Outline each blood parasite and name the species.
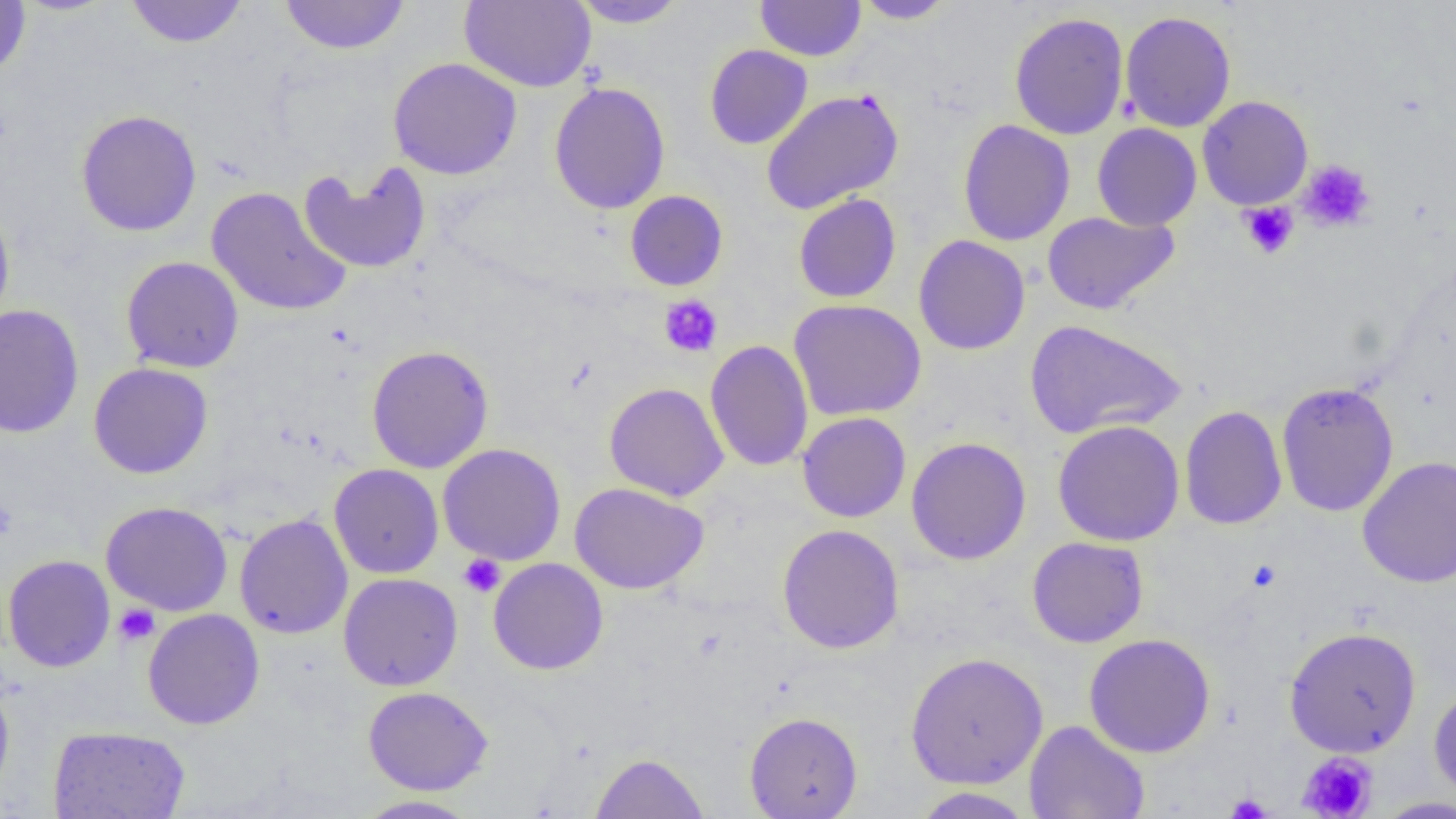
No blood parasites seen.

slide-level diagnosis = no evidence of blood parasites
platelet locations = approximate bounding boxes as named x1/y1/x2/y2 corners in pixels: (x1=1298, y1=160, x2=1376, y2=233), (x1=1238, y1=201, x2=1299, y2=260), (x1=658, y1=294, x2=723, y2=358), (x1=0, y1=497, x2=18, y2=541), (x1=458, y1=554, x2=506, y2=597), (x1=114, y1=604, x2=160, y2=646), (x1=1298, y1=752, x2=1377, y2=818), (x1=1226, y1=793, x2=1272, y2=818)
modality = optical microscopy
uninfected red blood cell locations = approximate bounding boxes as named x1/y1/x2/y2 corners in pixels: (x1=124, y1=0, x2=249, y2=49), (x1=280, y1=0, x2=410, y2=55), (x1=459, y1=0, x2=596, y2=92), (x1=570, y1=0, x2=689, y2=28), (x1=755, y1=0, x2=866, y2=61), (x1=853, y1=0, x2=957, y2=24), (x1=0, y1=1, x2=31, y2=78), (x1=1120, y1=10, x2=1236, y2=133), (x1=1009, y1=12, x2=1129, y2=140), (x1=704, y1=44, x2=813, y2=149), (x1=388, y1=57, x2=523, y2=179), (x1=549, y1=82, x2=671, y2=214), (x1=761, y1=88, x2=903, y2=215), (x1=1197, y1=95, x2=1313, y2=210), (x1=75, y1=109, x2=202, y2=237), (x1=958, y1=119, x2=1075, y2=247), (x1=1091, y1=123, x2=1202, y2=231), (x1=298, y1=161, x2=432, y2=274), (x1=206, y1=186, x2=352, y2=317), (x1=625, y1=190, x2=728, y2=291), (x1=793, y1=194, x2=902, y2=303), (x1=0, y1=199, x2=15, y2=330), (x1=1042, y1=210, x2=1179, y2=314), (x1=914, y1=235, x2=1030, y2=355), (x1=121, y1=255, x2=244, y2=373), (x1=788, y1=299, x2=926, y2=421), (x1=0, y1=304, x2=84, y2=439), (x1=1024, y1=319, x2=1186, y2=440), (x1=705, y1=340, x2=814, y2=471), (x1=366, y1=344, x2=494, y2=474), (x1=88, y1=362, x2=214, y2=479), (x1=1276, y1=381, x2=1399, y2=517), (x1=604, y1=382, x2=729, y2=502), (x1=1179, y1=405, x2=1287, y2=530), (x1=797, y1=411, x2=912, y2=523), (x1=1052, y1=420, x2=1184, y2=546), (x1=906, y1=436, x2=1031, y2=565), (x1=438, y1=443, x2=567, y2=566), (x1=1357, y1=456, x2=1456, y2=588), (x1=329, y1=463, x2=444, y2=579), (x1=570, y1=481, x2=709, y2=594), (x1=100, y1=501, x2=233, y2=616), (x1=234, y1=513, x2=353, y2=639), (x1=777, y1=524, x2=905, y2=654), (x1=1027, y1=536, x2=1149, y2=648), (x1=2, y1=554, x2=116, y2=672), (x1=487, y1=558, x2=609, y2=675), (x1=338, y1=572, x2=463, y2=691), (x1=142, y1=608, x2=265, y2=729), (x1=1283, y1=626, x2=1422, y2=757), (x1=1083, y1=633, x2=1216, y2=758), (x1=904, y1=651, x2=1049, y2=790), (x1=0, y1=675, x2=15, y2=802), (x1=1428, y1=684, x2=1456, y2=802), (x1=362, y1=686, x2=494, y2=796), (x1=744, y1=711, x2=863, y2=818), (x1=1024, y1=720, x2=1149, y2=819), (x1=48, y1=725, x2=191, y2=819), (x1=590, y1=752, x2=709, y2=818), (x1=909, y1=787, x2=1035, y2=818), (x1=353, y1=794, x2=481, y2=818), (x1=1372, y1=796, x2=1456, y2=818)
preparation = thin blood smear
magnification = 1000x
image size = 1456×819 pixels
field of view = single